State which parasite is depicted.
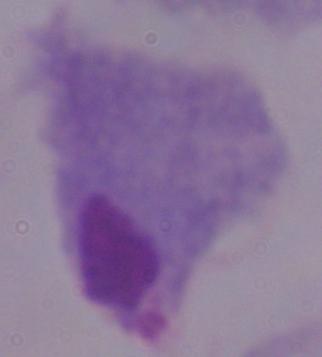
This is a trichomonad.

modality = micrograph
magnification = 1000x